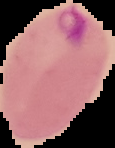

image type = segmented cell region on a black background
malaria status = parasitized
preparation = thin blood smear
image size = 115×148 pixels